Classify this cell by malaria status.
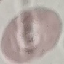

It is uninfected.

Automatically extracted cell patch, resized to 64 × 64 pixels. Thin blood smear. Giemsa stain. Acquired by smartphone through the microscope eyepiece.